Give the position of every malaria parasite.
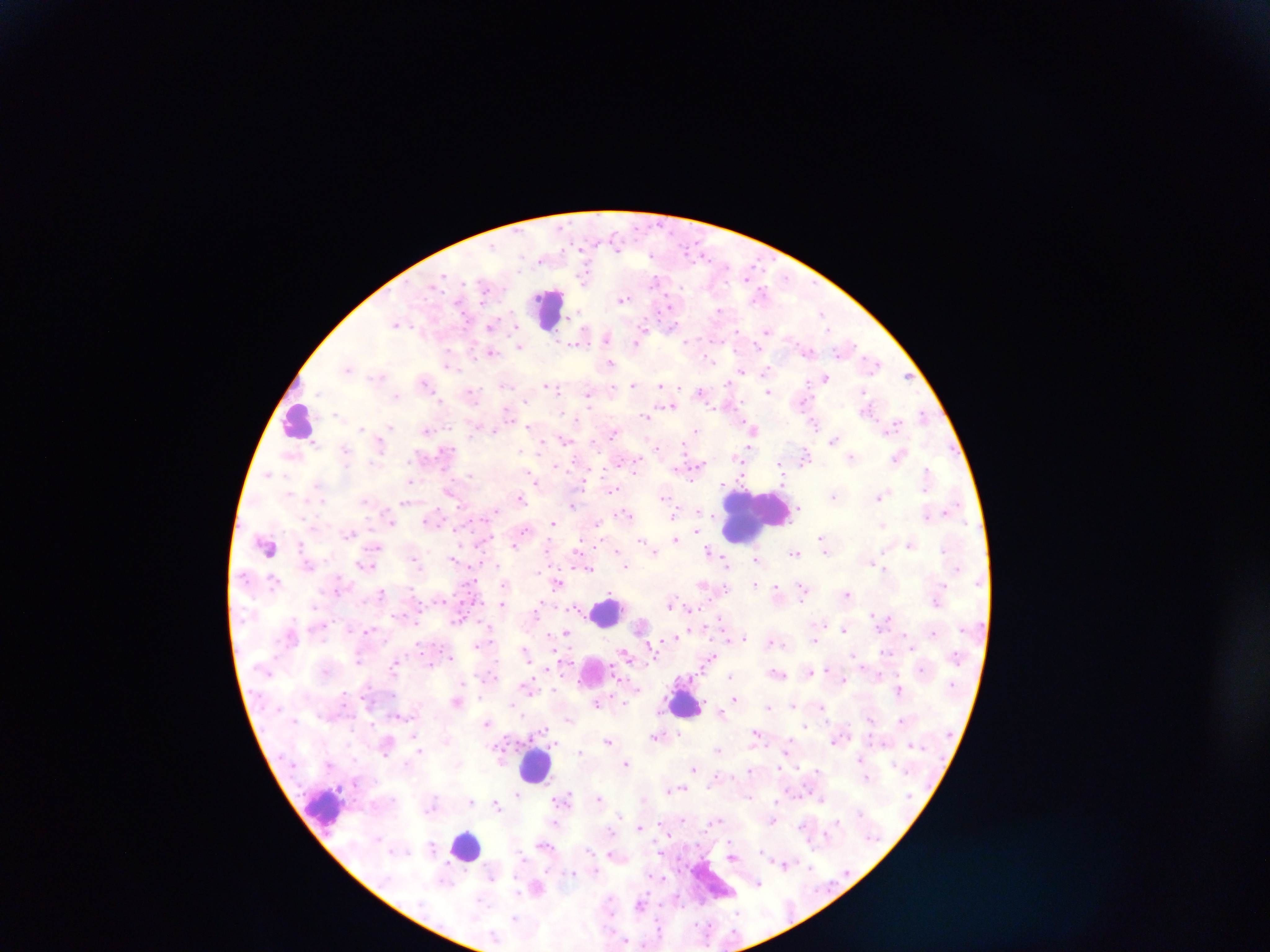
Approximate centers as [x, y] in pixels.
Malaria parasites: [622, 298], [720, 311], [823, 311], [397, 323], [672, 326], [491, 327], [767, 330], [643, 332], [607, 336], [640, 339], [519, 345], [491, 351], [449, 357], [873, 361], [610, 363], [348, 367], [768, 370], [741, 372], [907, 376], [825, 379], [425, 382], [633, 384], [549, 385], [662, 385], [554, 387], [767, 390], [701, 392], [471, 393], [589, 393], [803, 401], [668, 405], [867, 408], [923, 414], [645, 416], [894, 423], [815, 424], [390, 427], [360, 428], [494, 429], [753, 429], [427, 430], [696, 433], [834, 439], [564, 440], [379, 442], [542, 443], [748, 450], [805, 456], [898, 456], [852, 457], [701, 465], [741, 466], [268, 474], [928, 474], [533, 476], [409, 481], [583, 481], [723, 482], [449, 491], [879, 495], [665, 496], [834, 496], [521, 498], [405, 502], [573, 504], [496, 511], [948, 511], [625, 513], [927, 514], [674, 515], [430, 519], [392, 520], [599, 521], [553, 522], [882, 524], [525, 529], [695, 529], [350, 533], [823, 536], [676, 539], [641, 540], [911, 543], [514, 544], [376, 546], [267, 547], [654, 550], [616, 551], [710, 552], [794, 552], [756, 558], [454, 559], [416, 560], [873, 562], [363, 565], [727, 565], [625, 567], [588, 568], [558, 582], [703, 583], [505, 584], [756, 584], [777, 588], [803, 588], [382, 591], [847, 592], [503, 604], [671, 604], [689, 606], [538, 611], [720, 618], [882, 618], [642, 625], [844, 628], [367, 630], [934, 630], [566, 632], [550, 635], [677, 637], [815, 638], [742, 639], [772, 641], [478, 644], [525, 651], [626, 653], [712, 657], [562, 661], [396, 662], [863, 667], [326, 670], [810, 670], [830, 671], [777, 673], [732, 677], [844, 679], [527, 686], [899, 689], [734, 698], [458, 701], [624, 701], [598, 702], [513, 703], [793, 704], [820, 707], [768, 708], [721, 711], [399, 715], [570, 718], [487, 723], [806, 725], [756, 731], [415, 734], [678, 734], [656, 735], [608, 739], [836, 740], [788, 747], [718, 749], [419, 751], [580, 751], [387, 752], [861, 758], [626, 763], [694, 768], [750, 770], [867, 776], [717, 777], [673, 789], [517, 794], [599, 797], [821, 798], [644, 799], [562, 800], [471, 802], [497, 805], [619, 813], [717, 819], [837, 820], [773, 821], [639, 827], [545, 845], [432, 847], [613, 854], [733, 856], [784, 863], [573, 872], [661, 876], [493, 877], [758, 883], [537, 887], [641, 904], [514, 918].

Summary:
  - Leukocyte locations: [549, 309], [299, 419], [755, 515], [607, 611], [592, 670], [685, 702], [535, 766], [325, 809], [467, 847], [713, 882]
  - Field of view: single
  - Country: Ghana
  - Image size: 1270×952 pixels
  - Preparation: thick blood film
  - Capture: mobile-phone photograph through a microscope